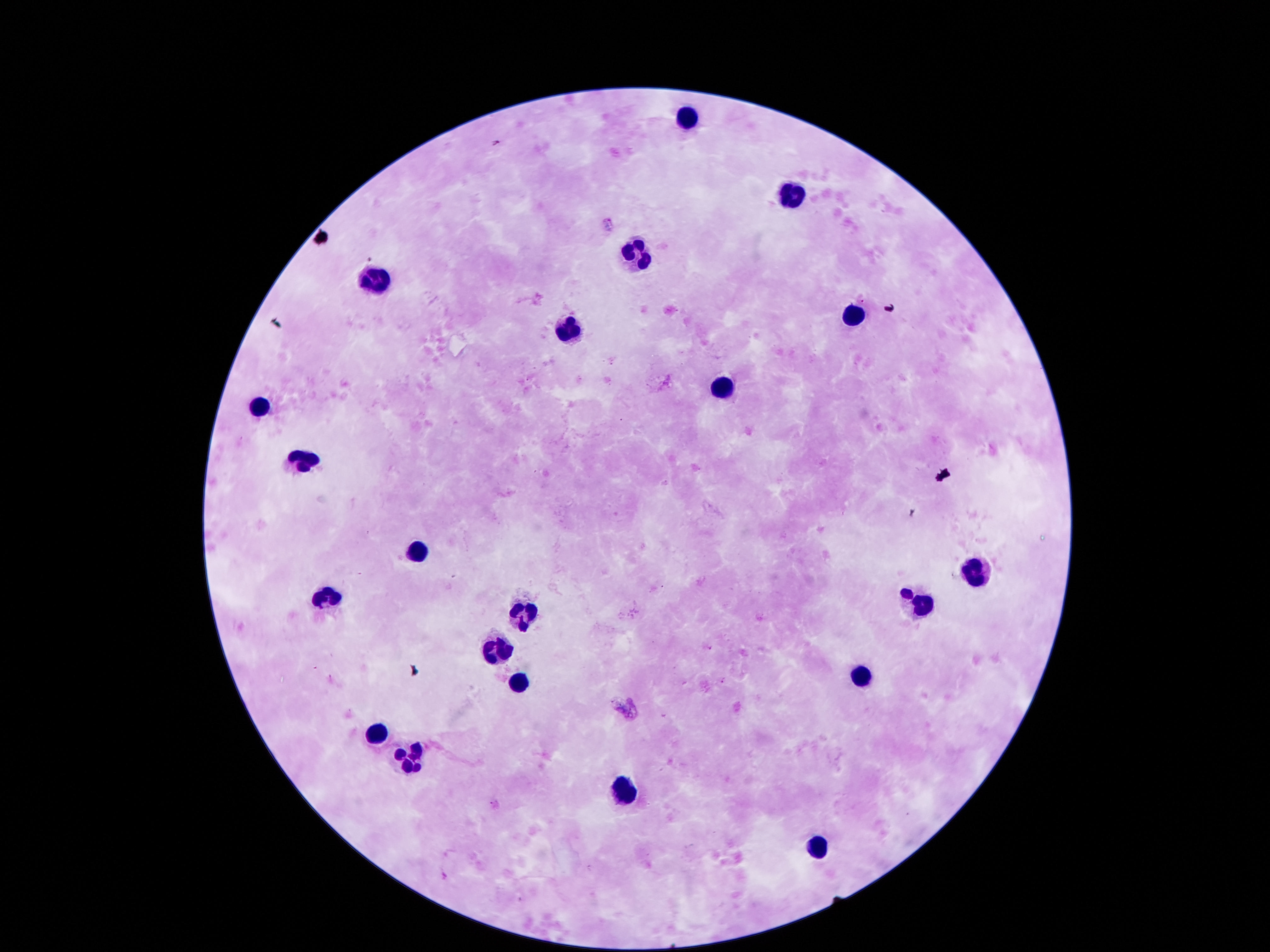

stain = Giemsa
preparation = thick peripheral-blood smear
capture = smartphone camera through the microscope eyepiece
image size = 1270×952 pixels
magnification = 100x
leukocyte locations = approximate centers as (x, y) in pixels: (685, 116), (795, 197), (633, 252), (381, 283), (845, 316), (566, 330), (723, 385), (259, 408), (302, 455), (413, 544), (975, 571), (326, 597), (914, 610), (523, 620), (500, 649), (862, 675), (523, 686), (375, 733), (407, 758), (624, 788), (816, 843)
patient malaria status = not infected
field of view = single